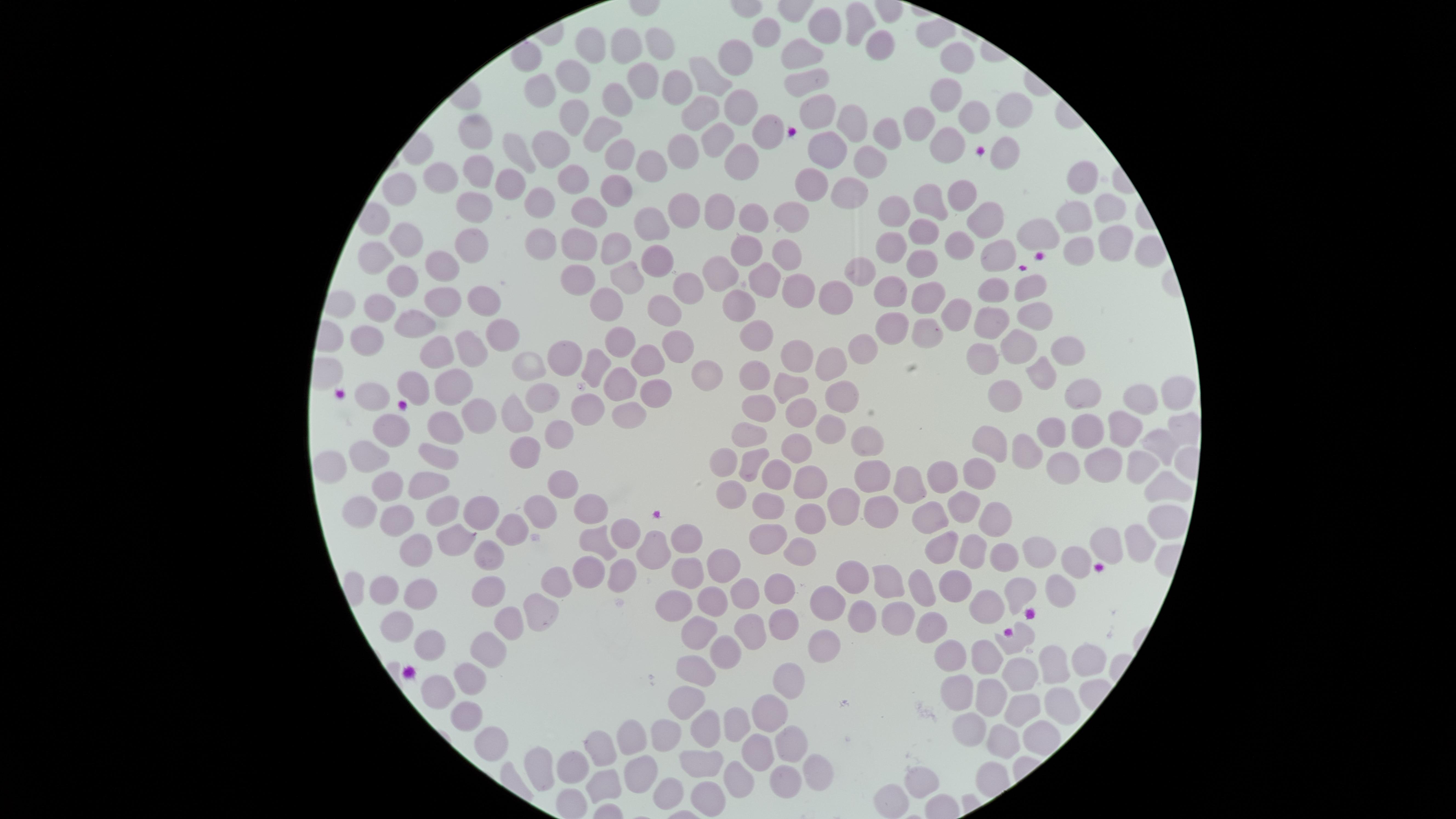 Approximate marker points as {x, y} in pixels. Uninfected red blood cells: {856, 23}, {821, 27}, {768, 30}, {658, 41}, {591, 46}, {877, 47}, {625, 48}, {737, 55}, {795, 56}, {958, 60}, {573, 74}, {713, 75}, {644, 76}, {806, 79}, {676, 81}, {540, 87}, {943, 94}, {616, 99}, {695, 108}, {817, 108}, {733, 110}, {1016, 110}, {571, 113}, {972, 118}, {918, 123}, {849, 124}, {600, 127}, {482, 129}, {761, 132}, {889, 133}, {721, 142}, {942, 148}, {519, 149}, {619, 149}, {1001, 149}, {684, 151}, {824, 151}, {549, 152}, {647, 159}, {738, 161}, {874, 161}, {474, 172}, {443, 175}, {1081, 179}, {501, 180}, {572, 183}, {815, 187}, {403, 188}, {617, 191}, {958, 191}, {848, 193}, {540, 200}, {928, 202}, {475, 203}, {684, 205}, {895, 207}, {593, 208}, {1104, 208}, {714, 210}, {791, 213}, {1077, 215}, {753, 218}, {654, 220}, {987, 223}, {1042, 229}, {474, 233}, {924, 234}, {407, 235}, {955, 241}, {1107, 241}, {577, 242}, {545, 243}, {620, 243}, {888, 247}, {377, 250}, {1076, 250}, {996, 251}, {789, 253}, {741, 254}, {656, 260}, {440, 263}, {920, 264}, {720, 269}, {863, 269}, {628, 274}, {575, 275}, {403, 280}, {765, 281}, {690, 283}, {797, 289}, {892, 289}, {1031, 289}, {995, 294}, {608, 296}, {833, 296}, {930, 297}, {479, 300}, {437, 304}, {382, 306}, {665, 306}, {738, 307}, {1031, 312}, {954, 314}, {991, 315}, {419, 325}, {885, 326}, {499, 328}, {761, 332}, {918, 332}, {370, 340}, {616, 342}, {1018, 342}, {677, 344}, {859, 344}, {471, 347}, {434, 352}, {1072, 352}, {983, 354}, {795, 355}, {649, 358}, {565, 360}, {590, 364}, {832, 365}, {529, 368}, {761, 370}, {709, 374}, {1035, 375}, {453, 381}, {414, 382}, {622, 383}, {792, 384}, {548, 388}, {1011, 388}, {373, 390}, {1083, 391}, {1172, 391}, {840, 392}, {656, 395}, {1142, 399}, {758, 407}, {591, 410}, {801, 413}, {476, 415}, {517, 415}, {627, 417}, {832, 423}, {1181, 426}, {1126, 427}, {1087, 428}, {443, 430}, {1051, 430}, {392, 431}, {562, 431}, {746, 431}, {866, 433}, {988, 441}, {1162, 442}, {795, 444}, {1029, 444}, {370, 452}, {531, 453}, {435, 456}, {1133, 458}, {721, 460}, {753, 461}, {1057, 461}, {1096, 463}, {331, 465}, {952, 470}, {871, 473}, {979, 475}, {778, 477}, {426, 480}, {808, 480}, {565, 481}, {910, 482}, {386, 486}, {1168, 486}, {723, 492}, {840, 500}, {542, 505}, {589, 505}, {766, 505}, {962, 505}, {480, 508}, {354, 509}, {814, 513}, {444, 514}, {874, 516}, {933, 516}, {992, 517}, {394, 522}, {1160, 522}, {623, 532}, {506, 533}, {686, 537}, {452, 538}, {591, 539}, {1139, 539}, {1107, 540}, {760, 541}, {936, 545}, {800, 548}, {654, 549}, {413, 551}, {967, 551}, {1031, 551}, {487, 552}, {1004, 556}, {1075, 558}, {718, 560}, {621, 568}, {891, 573}, {579, 574}, {683, 574}, {854, 574}, {775, 581}, {953, 585}, {385, 586}, {919, 586}, {548, 589}, {740, 589}, {1015, 589}, {1050, 594}, {486, 597}, {671, 599}, {413, 600}, {825, 602}, {703, 603}, {985, 605}, {539, 613}, {858, 613}, {781, 618}, {893, 618}, {396, 619}, {929, 625}, {507, 626}, {752, 626}, {694, 633}, {1018, 637}, {429, 643}, {824, 643}, {951, 645}, {729, 651}, {493, 655}, {984, 656}, {1083, 661}, {1055, 667}, {1020, 672}, {468, 674}, {694, 674}, {953, 682}, {784, 688}, {435, 694}, {994, 697}, {686, 699}, {1065, 700}, {1019, 710}, {468, 714}, {764, 718}, {729, 721}, {710, 726}, {970, 729}, {669, 731}, {1038, 732}, {630, 735}, {1002, 736}, {490, 738}, {793, 744}, {598, 750}, {758, 752}, {703, 762}, {572, 764}, {536, 766}, {817, 767}, {639, 769}, {742, 771}, {786, 774}, {920, 778}, {606, 783}. Thin blood film. Presence: no malaria parasites detected. Giemsa-stained preparation. Photographed with a smartphone camera through the microscope eyepiece. One field of view of the specimen. Image is 1456×819 pixels. Circular visible region.